Identify the blood parasite species.
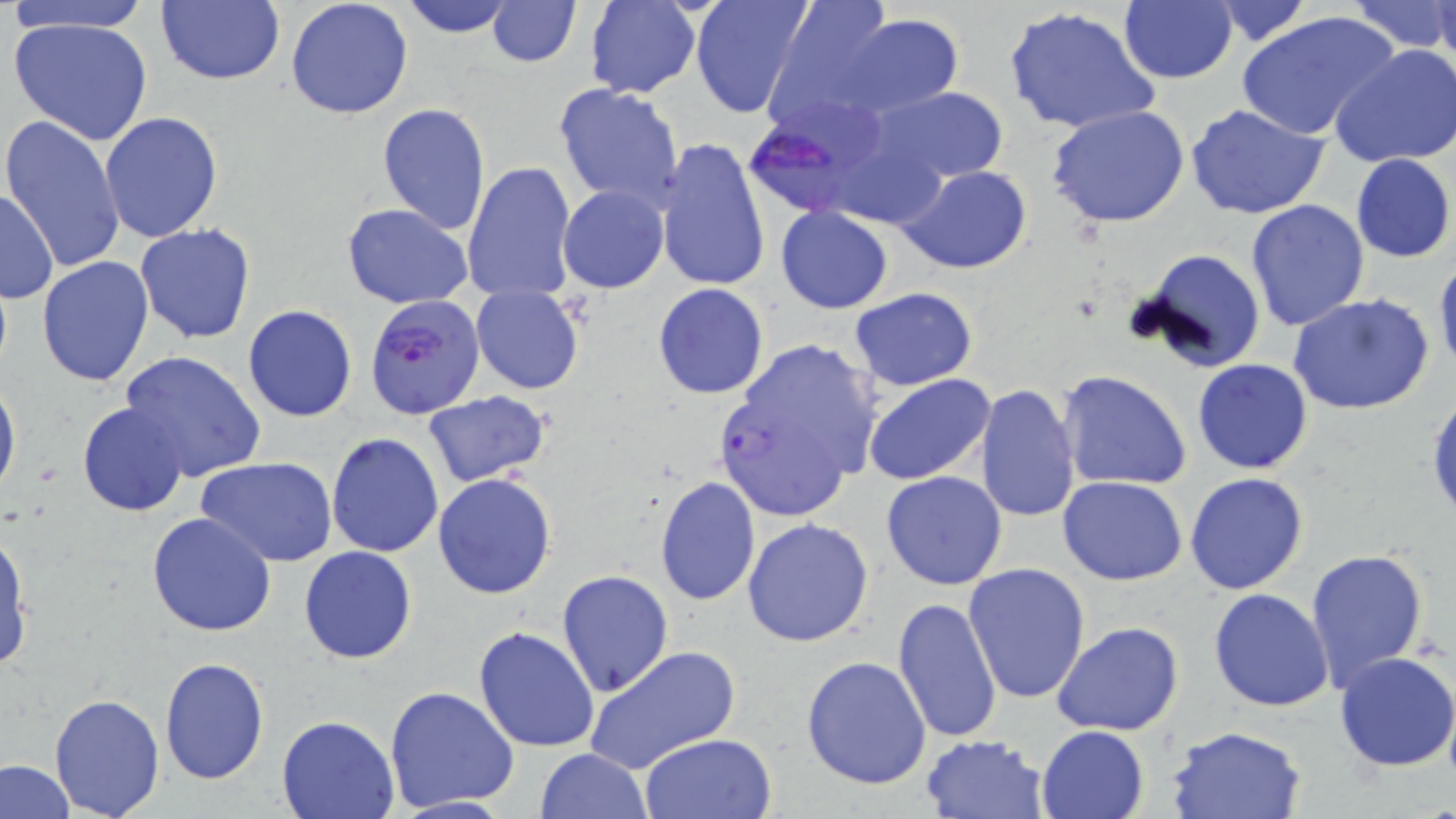
Plasmodium falciparum.

Summary:
  - Coordinate format: approximate bounding boxes as (x1, y1, x2, y2) in pixels
  - Plasmodium falciparum-infected red blood cell locations: (740, 92, 897, 225), (365, 295, 485, 420), (721, 396, 855, 520)
  - Uninfected red blood cell locations: (2, 0, 157, 33), (156, 0, 285, 88), (285, 0, 415, 121), (398, 0, 519, 37), (486, 0, 581, 67), (688, 0, 812, 119), (583, 1, 702, 99), (763, 1, 899, 125), (1200, 1, 1313, 47), (1348, 1, 1453, 54), (1118, 2, 1238, 84), (1432, 2, 1456, 71), (1004, 6, 1161, 136), (1237, 10, 1400, 142), (838, 13, 963, 116), (8, 15, 156, 146), (1331, 46, 1456, 169), (554, 82, 685, 207), (875, 87, 1009, 185), (376, 102, 492, 234), (1186, 104, 1331, 219), (1046, 105, 1192, 230), (99, 112, 224, 245), (2, 114, 127, 272), (655, 138, 772, 296), (1351, 153, 1455, 264), (463, 162, 578, 304), (898, 165, 1033, 275), (0, 186, 59, 304), (558, 186, 668, 293), (1244, 199, 1370, 333), (341, 203, 474, 309), (775, 206, 893, 314), (134, 224, 257, 344), (1128, 248, 1268, 375), (1434, 253, 1456, 382), (36, 257, 156, 388), (470, 283, 585, 393), (653, 283, 769, 399), (849, 287, 979, 392), (1288, 292, 1436, 415), (243, 304, 358, 422), (755, 342, 879, 475), (119, 349, 267, 483), (1192, 359, 1314, 474), (0, 371, 20, 505), (1058, 371, 1192, 492), (864, 374, 996, 486), (975, 384, 1081, 523), (422, 390, 550, 488), (1426, 390, 1456, 527), (77, 402, 189, 516), (326, 432, 446, 558), (198, 459, 337, 567), (880, 472, 1008, 591), (1185, 472, 1309, 594), (432, 473, 558, 600), (654, 475, 761, 605), (1057, 477, 1188, 586), (146, 512, 277, 638), (742, 518, 875, 648), (0, 528, 31, 673), (299, 546, 417, 664), (1306, 549, 1430, 693), (962, 562, 1092, 706), (557, 571, 674, 697), (1208, 589, 1334, 712), (891, 597, 1002, 744), (1052, 622, 1184, 735), (474, 626, 602, 752), (585, 646, 740, 775), (1334, 650, 1456, 775), (159, 657, 269, 784), (801, 657, 932, 790), (383, 684, 521, 813), (49, 693, 166, 818), (277, 713, 399, 818), (1165, 725, 1309, 819), (1036, 726, 1150, 819), (639, 732, 776, 819), (919, 732, 1050, 819), (535, 747, 652, 819), (0, 759, 75, 819)
  - Magnification: 1000x
  - Modality: optical microscopy
  - Image size: 1456×819 pixels
  - Stain: May-Grünwald-Giemsa
  - Preparation: thin blood smear
  - Field of view: single